Report the malaria status of this cell.
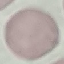

Uninfected.

Acquired by smartphone through the microscope eyepiece. Thin blood smear. Cell patch, automatically extracted from a larger field of view and resized to 64 × 64 pixels. Giemsa stain.